Describe the morphology of the red blood cells.
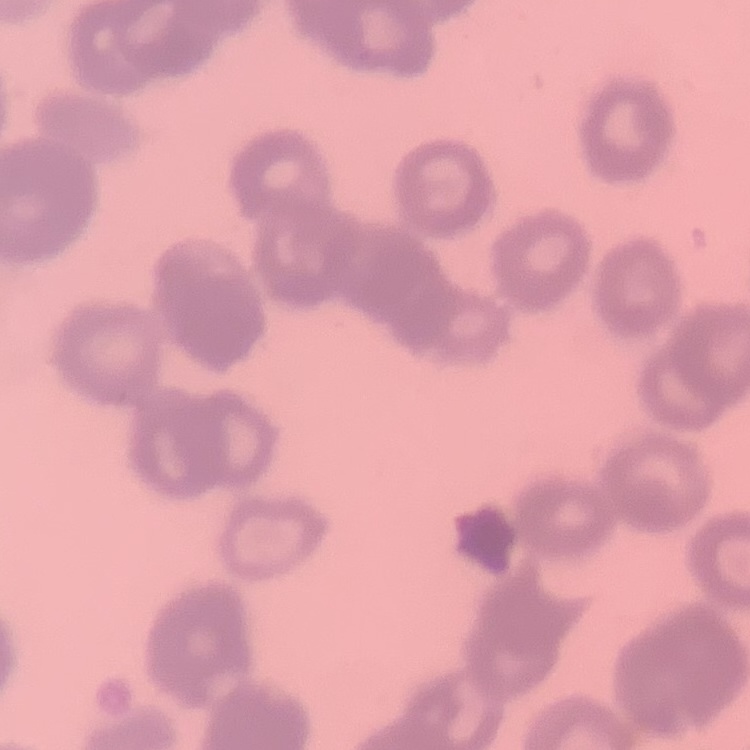
Rouleaux formation.

Field's or Giemsa stain. Thin blood smear. Square crop of a larger photomicrograph.